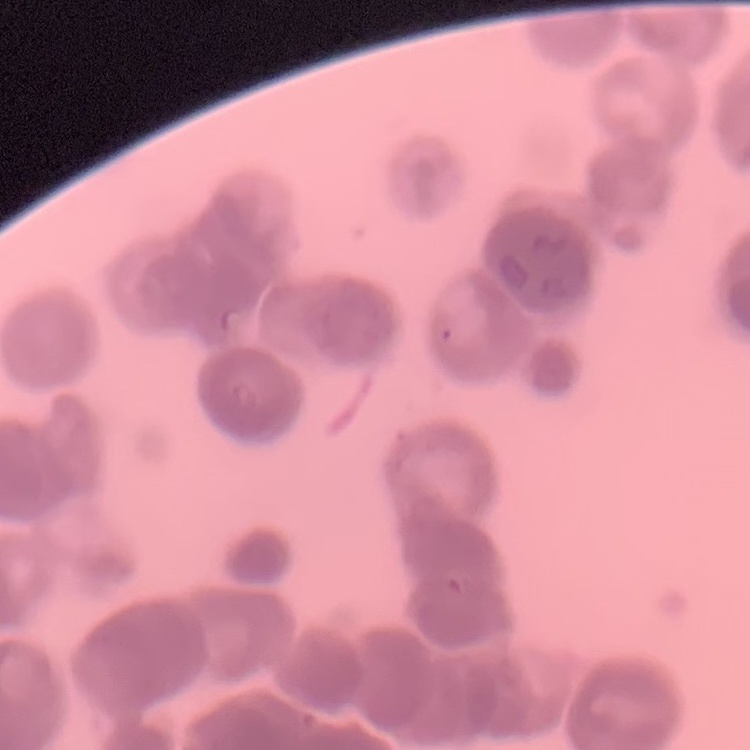
Summary:
  - Erythrocyte morphology: rouleaux formation
  - Image type: one tile cut from a larger photomicrograph
  - Stain: Field's or Giemsa
  - Preparation: thin blood film